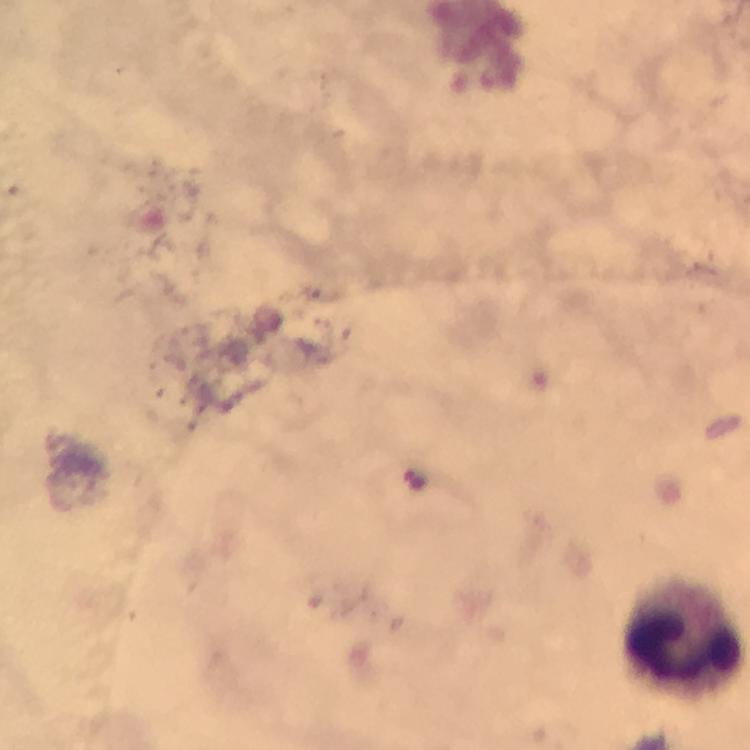
Approximate centers as (x, y) in pixels.
Summary:
  - Leukocyte locations: (682, 634)
  - Cropped from: a single field of view
  - Context: from a malaria diagnostic workup
  - Capture: smartphone mounted on the microscope
  - Stain: Giemsa
  - Preparation: thick smear
  - Immersion oil: used
  - Plasmodium parasites: none detected
  - Magnification: 100x
  - Image size: 750×750 pixels